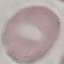

Summary:
  - Result: negative for malaria parasites
  - Preparation: thin blood smear
  - Stain: Giemsa
  - Capture: smartphone through the microscope eyepiece
  - Image type: automatically extracted cell patch, resized to 64 × 64 pixels